Outline platelets.
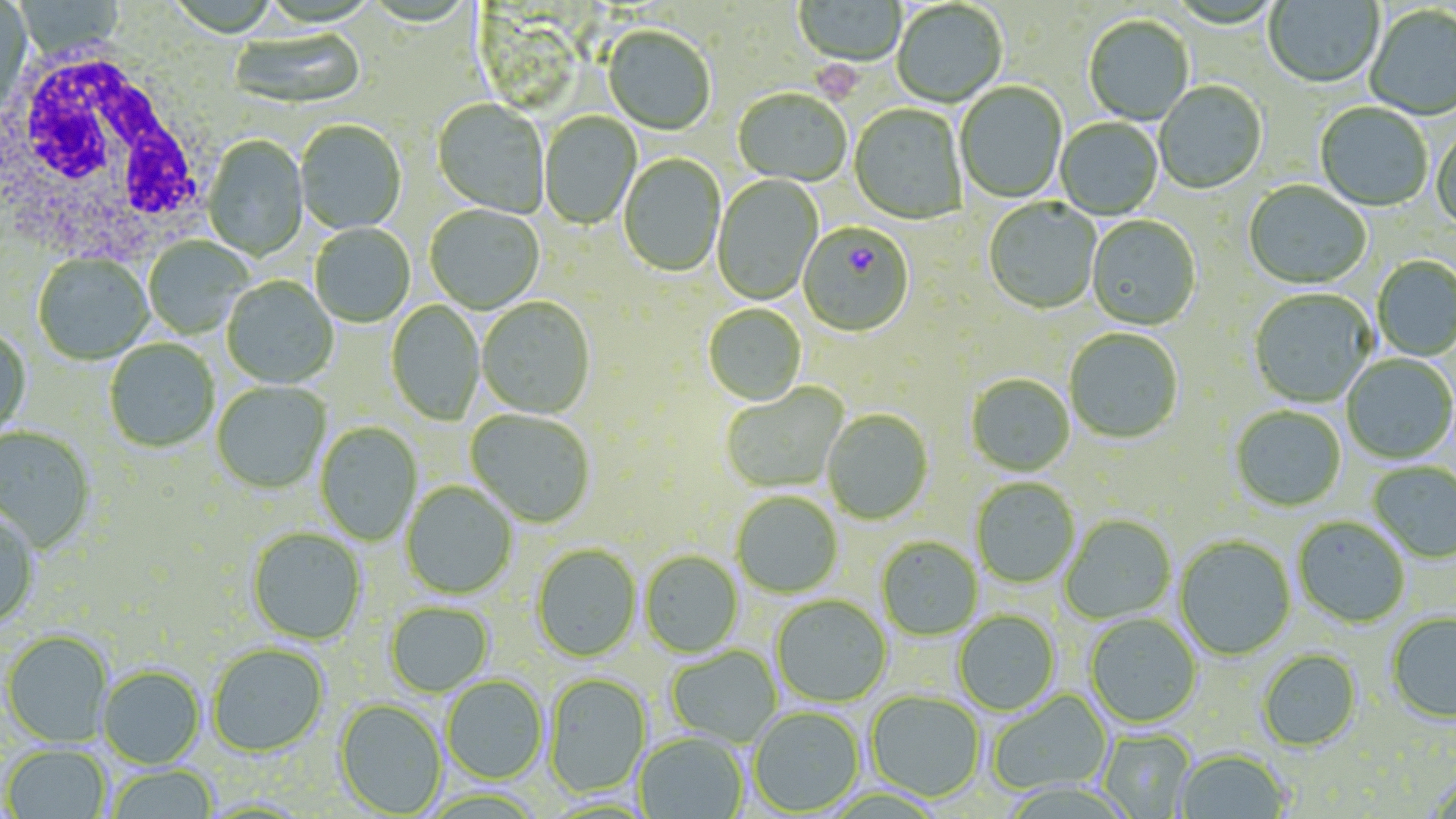
Approximate bounding boxes as named x1/y1/x2/y2 corners in pixels.
Platelets: (x1=810, y1=53, x2=867, y2=105).

Uninfected red blood cell locations: (x1=0, y1=0, x2=32, y2=115), (x1=1263, y1=0, x2=1383, y2=90), (x1=14, y1=1, x2=126, y2=61), (x1=794, y1=1, x2=907, y2=68), (x1=892, y1=2, x2=1007, y2=108), (x1=1364, y1=6, x2=1456, y2=121), (x1=1083, y1=16, x2=1194, y2=126), (x1=602, y1=27, x2=715, y2=136), (x1=229, y1=29, x2=366, y2=111), (x1=955, y1=82, x2=1067, y2=204), (x1=1155, y1=82, x2=1267, y2=195), (x1=733, y1=90, x2=851, y2=187), (x1=432, y1=99, x2=549, y2=219), (x1=1315, y1=104, x2=1432, y2=212), (x1=849, y1=105, x2=967, y2=226), (x1=539, y1=113, x2=640, y2=230), (x1=1055, y1=118, x2=1163, y2=220), (x1=295, y1=121, x2=406, y2=235), (x1=1431, y1=126, x2=1456, y2=233), (x1=202, y1=136, x2=309, y2=261), (x1=619, y1=154, x2=725, y2=278), (x1=712, y1=174, x2=824, y2=306), (x1=1243, y1=181, x2=1371, y2=292), (x1=983, y1=199, x2=1102, y2=315), (x1=425, y1=205, x2=545, y2=314), (x1=1086, y1=216, x2=1201, y2=332), (x1=310, y1=224, x2=415, y2=327), (x1=144, y1=237, x2=252, y2=339), (x1=33, y1=255, x2=153, y2=365), (x1=1372, y1=256, x2=1456, y2=361), (x1=222, y1=277, x2=338, y2=389), (x1=1248, y1=290, x2=1377, y2=409), (x1=477, y1=298, x2=595, y2=420), (x1=386, y1=299, x2=485, y2=427), (x1=703, y1=305, x2=807, y2=407), (x1=0, y1=329, x2=31, y2=438), (x1=1064, y1=329, x2=1184, y2=445), (x1=104, y1=340, x2=218, y2=454), (x1=1341, y1=355, x2=1456, y2=464), (x1=965, y1=375, x2=1075, y2=477), (x1=212, y1=382, x2=330, y2=494), (x1=721, y1=385, x2=848, y2=494), (x1=1231, y1=406, x2=1346, y2=512), (x1=465, y1=410, x2=594, y2=527), (x1=822, y1=410, x2=933, y2=526), (x1=315, y1=422, x2=422, y2=546), (x1=0, y1=426, x2=95, y2=553), (x1=1368, y1=462, x2=1456, y2=563), (x1=970, y1=478, x2=1080, y2=589), (x1=401, y1=481, x2=518, y2=600), (x1=731, y1=493, x2=843, y2=599), (x1=0, y1=510, x2=40, y2=630), (x1=1060, y1=515, x2=1176, y2=624), (x1=1293, y1=516, x2=1410, y2=628), (x1=247, y1=529, x2=366, y2=645), (x1=1174, y1=536, x2=1296, y2=661), (x1=876, y1=537, x2=983, y2=641), (x1=531, y1=545, x2=641, y2=663), (x1=639, y1=551, x2=743, y2=659), (x1=772, y1=596, x2=891, y2=708), (x1=385, y1=603, x2=494, y2=697), (x1=953, y1=611, x2=1060, y2=716), (x1=1386, y1=612, x2=1456, y2=724), (x1=1084, y1=613, x2=1202, y2=729), (x1=2, y1=631, x2=112, y2=747), (x1=207, y1=644, x2=328, y2=756), (x1=666, y1=646, x2=782, y2=747), (x1=1256, y1=648, x2=1362, y2=751), (x1=98, y1=666, x2=205, y2=769), (x1=544, y1=675, x2=651, y2=799), (x1=441, y1=676, x2=548, y2=784), (x1=988, y1=689, x2=1112, y2=796), (x1=866, y1=691, x2=985, y2=803), (x1=334, y1=699, x2=447, y2=817), (x1=748, y1=707, x2=864, y2=816), (x1=1098, y1=730, x2=1196, y2=818), (x1=634, y1=732, x2=748, y2=819), (x1=3, y1=744, x2=110, y2=819), (x1=1175, y1=748, x2=1291, y2=818), (x1=105, y1=765, x2=218, y2=819). Plasmodium falciparum-infected red blood cell locations: (x1=798, y1=224, x2=914, y2=338). White blood cell locations: (x1=0, y1=45, x2=214, y2=265). Slide-level diagnosis: Plasmodium falciparum. Image is 1456×819 pixels. Single field of view. May-Grünwald-Giemsa stain. Thin blood film. 1000x magnification. Light microscopy.